Outline each blood parasite and name the species.
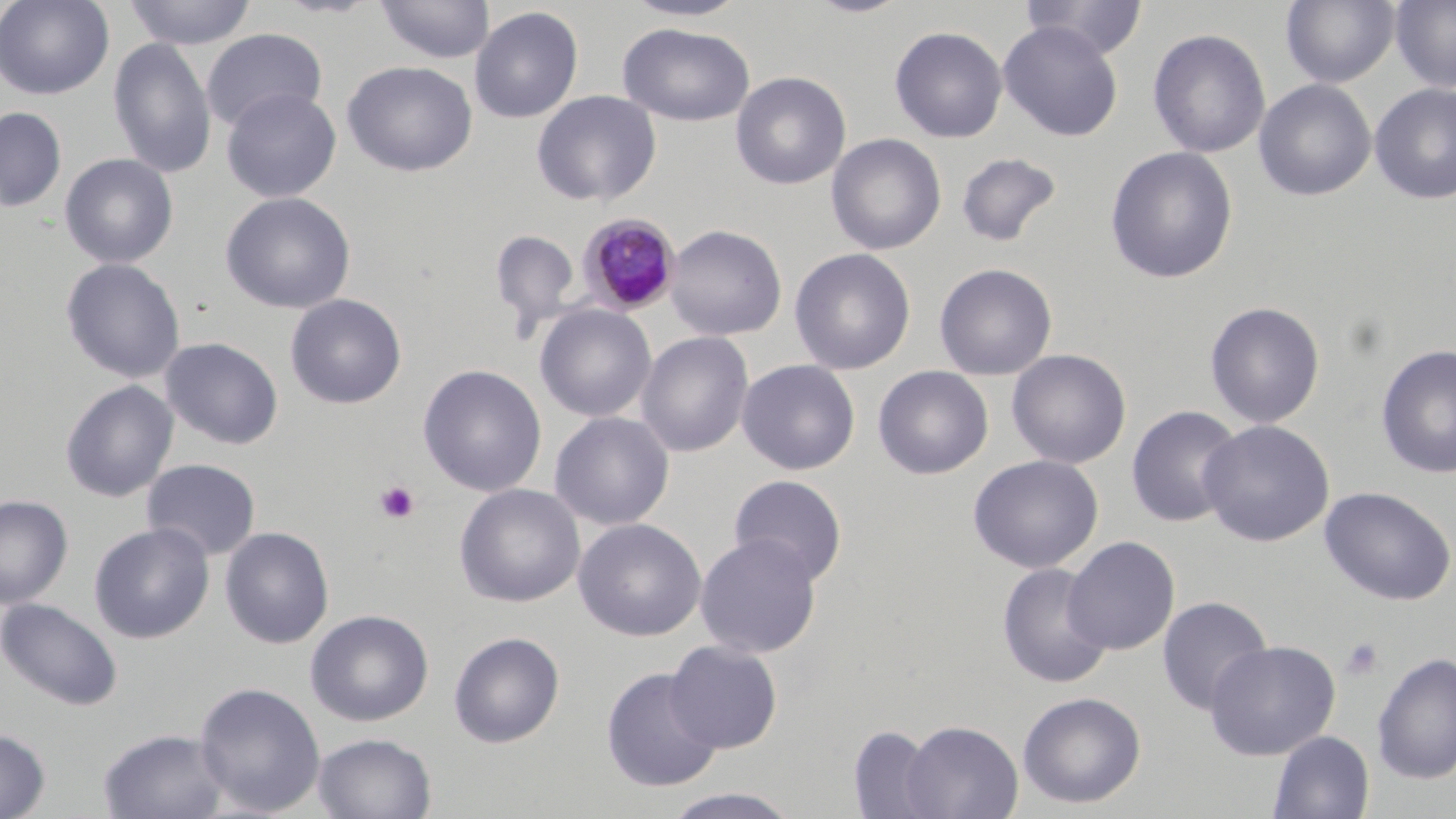
Approximate bounding boxes as (x1,y1)-(x2,y2) corner pairs in pixels.
Plasmodium malariae-infected red blood cells: (579,214)-(682,314).
No Plasmodium falciparum, Plasmodium ovale, Plasmodium vivax, Babesia divergens, or Trypanosoma brucei observed.

Summary:
  - Uninfected red blood cell locations: (0,0)-(115,100), (270,0)-(383,19), (621,0)-(751,22), (805,0)-(914,18), (1019,0)-(1149,60), (1280,0)-(1400,88), (1390,0)-(1456,92), (122,1)-(257,50), (375,1)-(495,65), (469,6)-(584,123), (998,21)-(1124,141), (618,22)-(755,126), (889,25)-(1008,143), (201,28)-(328,134), (1148,28)-(1271,159), (108,37)-(216,180), (342,60)-(478,176), (730,71)-(851,190), (1253,78)-(1377,201), (1370,83)-(1456,205), (221,87)-(341,203), (531,90)-(662,207), (0,107)-(67,212), (826,133)-(947,255), (1104,146)-(1239,284), (955,152)-(1062,248), (59,153)-(178,269), (220,191)-(356,314), (664,224)-(787,340), (490,229)-(580,337), (789,247)-(916,375), (60,258)-(185,384), (934,263)-(1057,380), (285,293)-(407,410), (1204,301)-(1326,428), (535,304)-(656,422), (636,331)-(754,458), (160,337)-(284,450), (1376,343)-(1456,480), (1006,349)-(1131,469), (737,359)-(860,475), (418,364)-(547,497), (872,366)-(994,480), (60,380)-(178,502), (1126,405)-(1244,527), (549,411)-(675,531), (1198,419)-(1335,547), (968,454)-(1104,573), (141,458)-(261,561), (728,474)-(849,586), (455,483)-(585,607), (1320,486)-(1455,606), (0,495)-(73,608), (573,517)-(706,642), (89,522)-(215,644), (220,526)-(335,649), (695,533)-(822,658), (1062,536)-(1180,655), (997,562)-(1112,689), (1156,596)-(1272,715), (1,598)-(123,711), (305,609)-(434,727), (449,631)-(565,747), (664,640)-(783,753), (1205,640)-(1341,760), (1372,651)-(1456,785), (601,667)-(722,792), (195,682)-(326,816), (1017,691)-(1146,809), (899,719)-(1023,819), (847,725)-(943,818), (0,728)-(50,818), (98,728)-(230,819), (1268,730)-(1374,819), (313,732)-(437,818), (660,787)-(804,819)
  - Platelet locations: (375,480)-(420,524), (1341,638)-(1384,680)
  - Slide-level diagnosis: Plasmodium malariae
  - Modality: optical microscopy
  - Stain: May-Grünwald-Giemsa
  - Field of view: one of a larger specimen
  - Image size: 1456×819 pixels
  - Magnification: 1000x
  - Preparation: thin blood smear